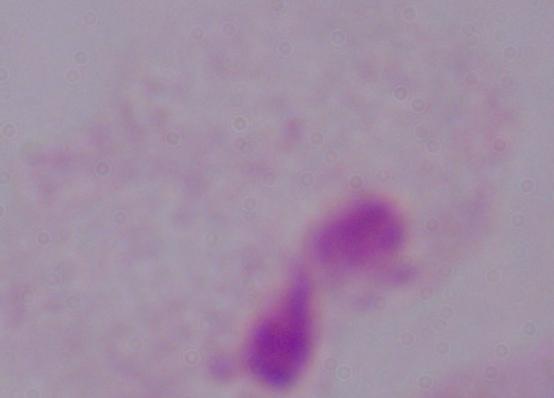
Summary:
  - Magnification: 1000x
  - Modality: micrograph
  - Identification: trichomonad